Point out each Plasmodium parasite.
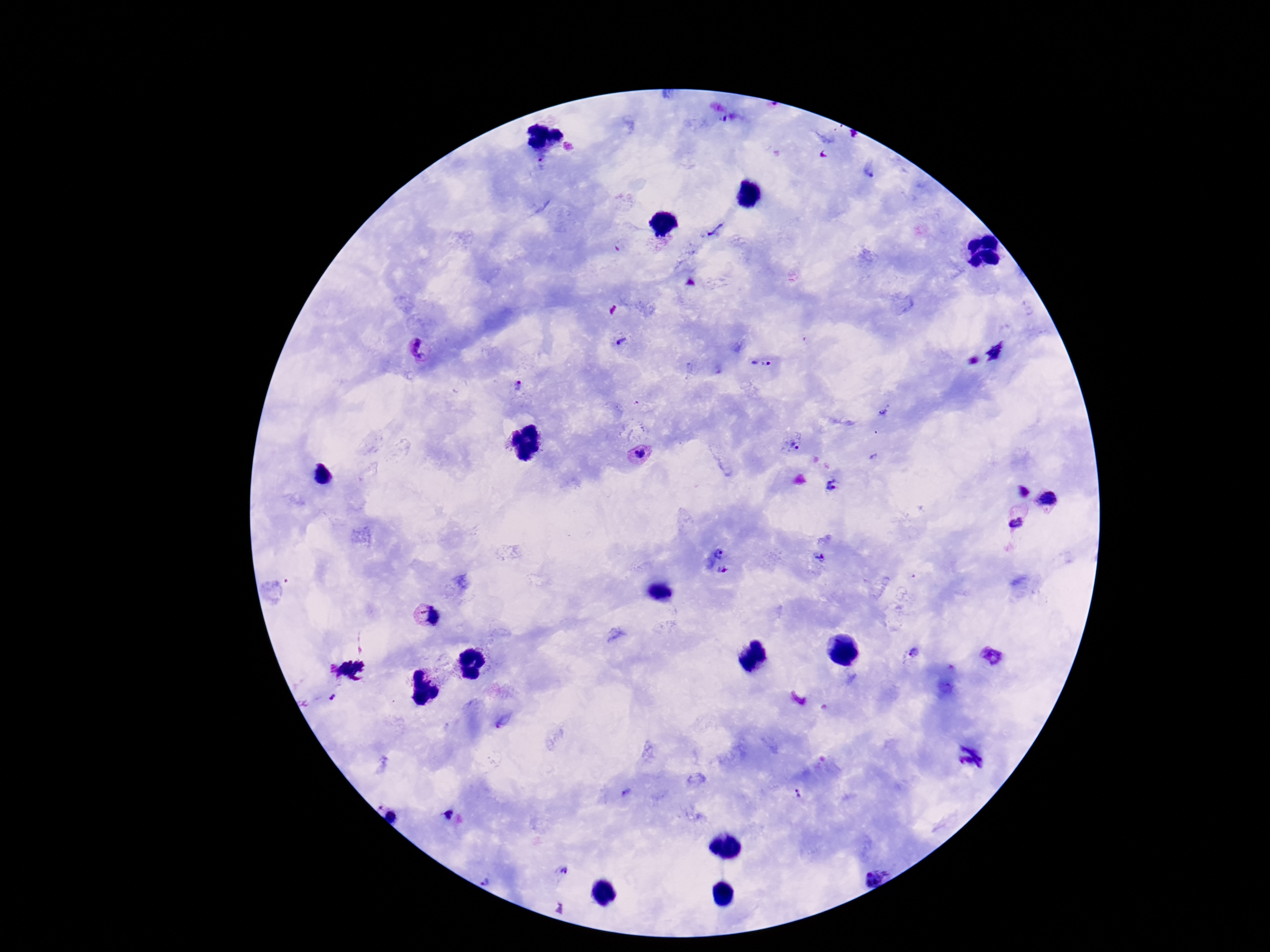

Approximate centers as [x, y] in pixels.
Plasmodium parasites: [868, 169], [715, 230], [621, 341], [421, 349], [762, 363], [515, 385], [884, 410], [791, 442], [641, 456], [833, 486], [1022, 490], [1050, 500], [1017, 518], [819, 557], [719, 561], [426, 613], [916, 653], [993, 656], [331, 697], [972, 757], [796, 794], [393, 814], [448, 814], [564, 871], [877, 876], [487, 880].

Thick blood film. Smartphone photograph taken through the microscope eyepiece. Image is 1270×952 pixels. Patient malaria status: positive. Giemsa-stained preparation. 100x magnification. Single field of view.